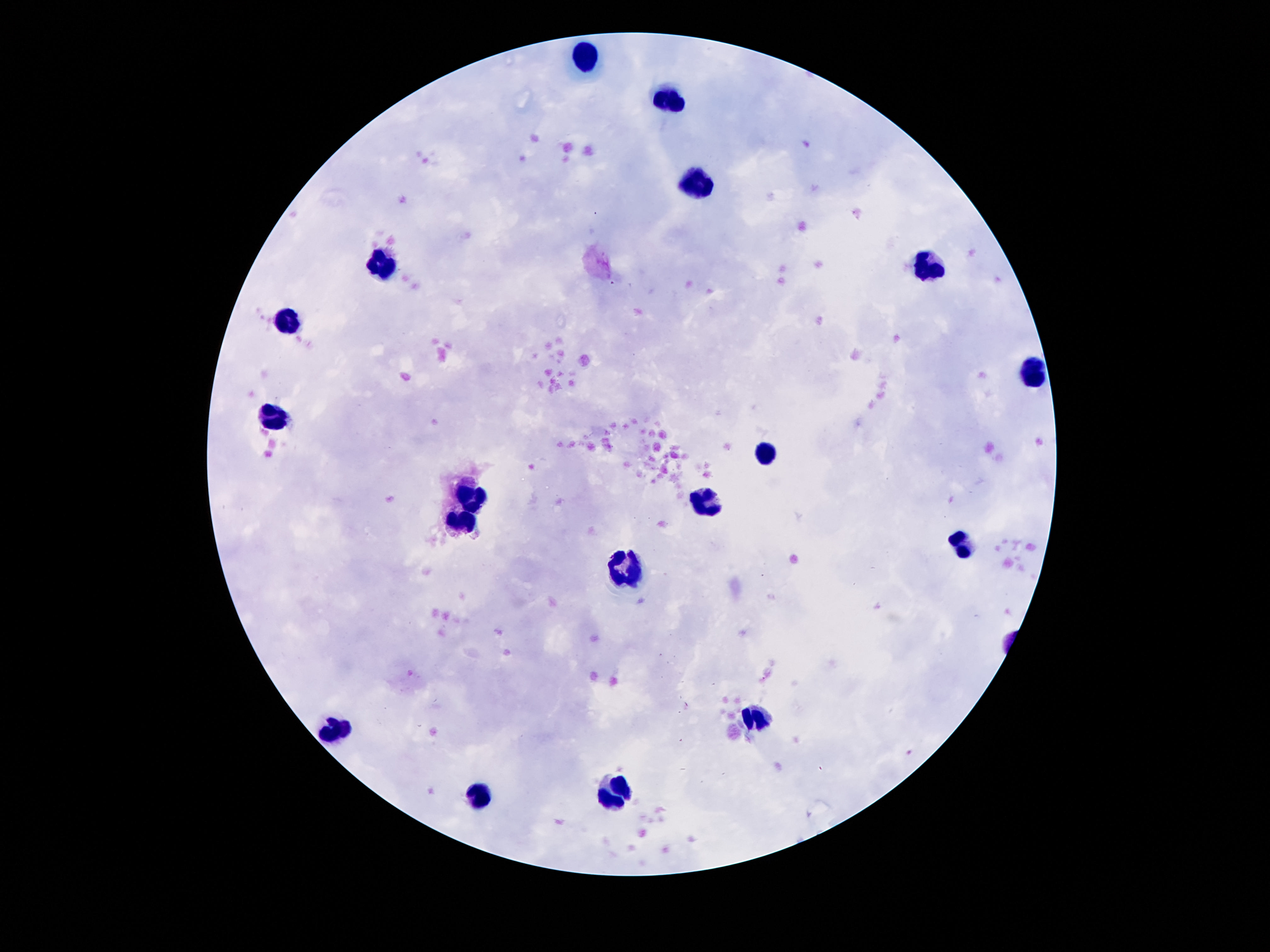

Approximate centers as {x, y} in pixels.
Summary:
  - Leukocyte locations: {587, 55}, {675, 100}, {696, 186}, {382, 262}, {927, 266}, {290, 321}, {1032, 374}, {274, 420}, {769, 454}, {468, 497}, {706, 502}, {464, 523}, {964, 544}, {624, 571}, {757, 715}, {337, 730}, {614, 791}, {477, 795}
  - Field of view: one from this slide
  - Preparation: thick blood smear
  - Image size: 1270×952 pixels
  - Capture: smartphone camera through the microscope eyepiece
  - Magnification: 100x
  - Patient malaria status: not infected
  - Stain: Giemsa